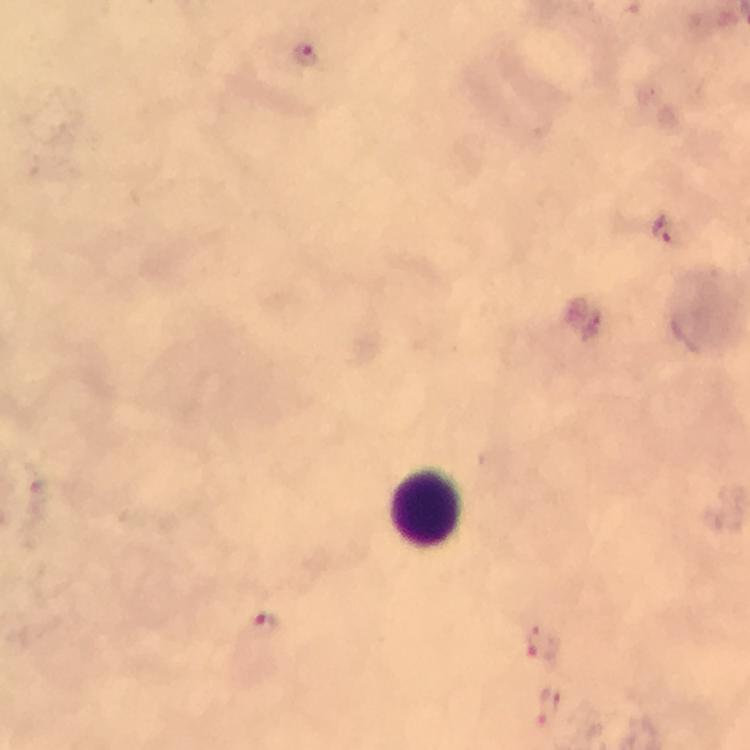
Approximate centers as {x, y} in pixels. Leukocyte locations: {426, 507}. Malaria parasite locations: {308, 55}, {666, 232}, {261, 624}, {542, 639}, {550, 709}. Smartphone photograph taken through a microscope. At 100x magnification. From a malaria diagnostic workup. Giemsa-stained preparation. Image is 750×750 pixels. Thick blood film. A crop from one field of view. Immersion oil applied.